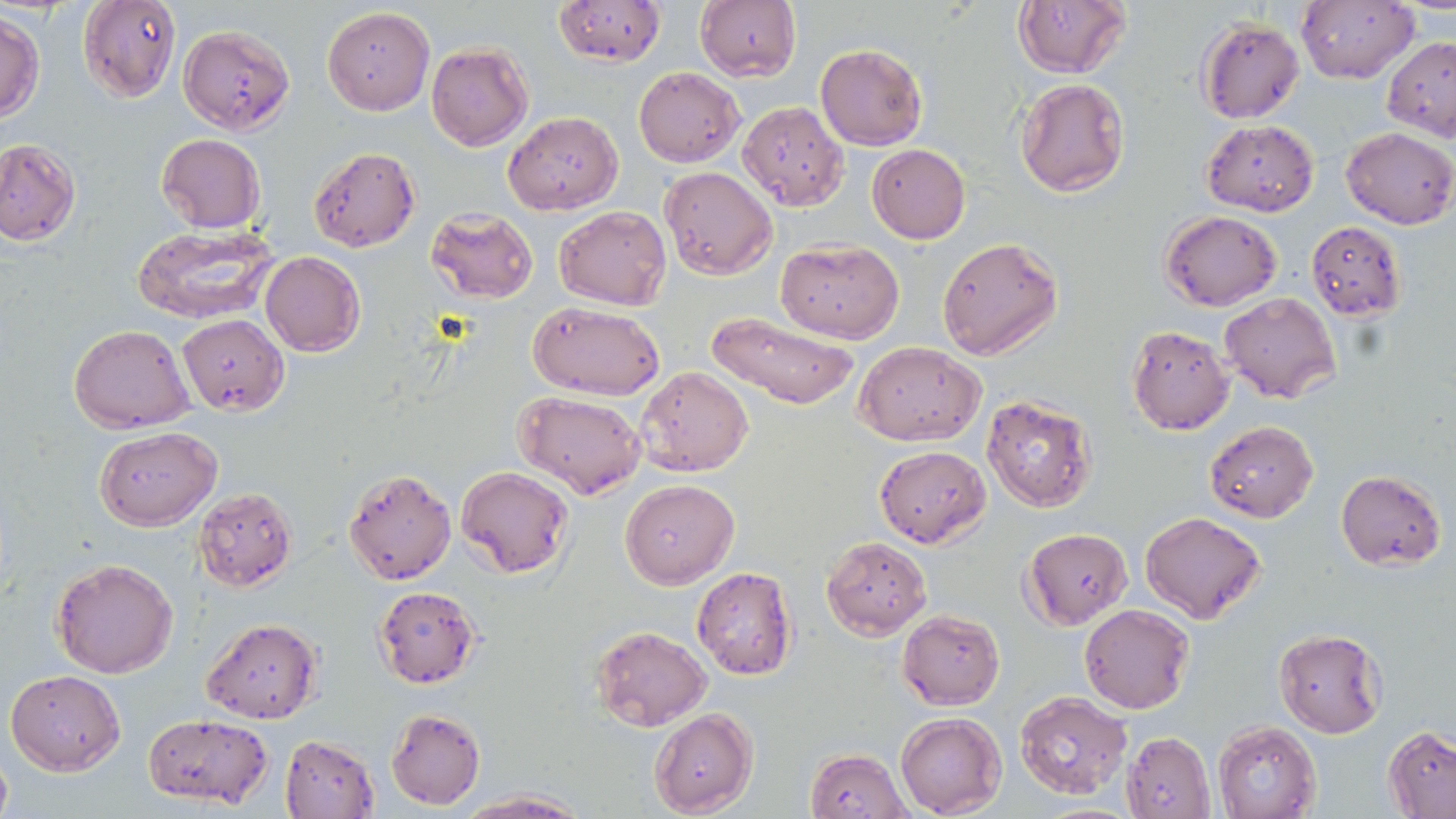
Approximate bounding boxes as (x1, y1, x2, y2) in pixels. Uninfected red blood cell locations: (78, 0, 183, 103), (551, 0, 668, 68), (1297, 0, 1417, 85), (695, 1, 801, 82), (1012, 2, 1130, 78), (322, 6, 435, 115), (0, 11, 44, 122), (1197, 17, 1305, 123), (179, 24, 295, 134), (1383, 36, 1456, 140), (425, 42, 532, 151), (815, 43, 927, 150), (633, 66, 744, 166), (1013, 78, 1130, 198), (738, 101, 850, 211), (504, 110, 622, 216), (1202, 120, 1319, 216), (1339, 126, 1454, 229), (157, 133, 265, 234), (0, 138, 80, 246), (866, 144, 971, 243), (308, 146, 420, 253), (659, 166, 776, 280), (555, 206, 670, 310), (426, 208, 539, 303), (1160, 210, 1282, 310), (1306, 220, 1407, 321), (133, 225, 278, 323), (937, 237, 1063, 360), (778, 238, 903, 344), (260, 252, 365, 356), (1221, 292, 1341, 404), (529, 301, 664, 401), (708, 312, 859, 411), (177, 314, 289, 415), (69, 323, 194, 433), (1126, 324, 1234, 434), (854, 341, 985, 446), (636, 366, 754, 477), (514, 391, 645, 498), (981, 394, 1098, 513), (1204, 419, 1319, 522), (94, 427, 221, 529), (874, 445, 990, 547), (342, 467, 455, 585), (457, 467, 573, 579), (1336, 470, 1446, 569), (619, 478, 738, 587), (193, 487, 298, 592), (1140, 511, 1268, 625), (1021, 527, 1132, 629), (822, 537, 932, 638), (51, 558, 179, 680), (692, 566, 797, 679), (371, 584, 482, 688), (1079, 604, 1195, 714), (898, 609, 1005, 710), (201, 617, 323, 724), (589, 626, 711, 731), (1273, 628, 1387, 737), (6, 669, 125, 774), (1015, 690, 1134, 801), (386, 707, 486, 810), (649, 709, 758, 816), (141, 712, 273, 811), (895, 712, 1006, 817), (1213, 720, 1321, 819), (1383, 725, 1456, 818), (1120, 731, 1215, 819), (280, 734, 379, 819), (0, 744, 13, 819), (805, 747, 911, 819), (456, 790, 588, 818). Slide-level diagnosis: Plasmodium falciparum. One field of a larger specimen. Image is 1456×819 pixels. May-Grünwald-Giemsa stain. Captured at 1000x magnification. Light microscopy. Thin blood smear.